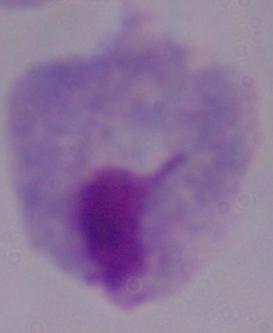
Micrograph. A trichomonad is shown. Captured at 1000x magnification.